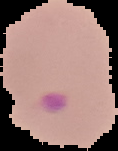
Summary:
  - Malaria status: parasitized
  - Image type: segmented cell region with the area outside set to black
  - Preparation: thin blood film
  - Image size: 118×151 pixels